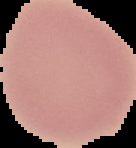

Summary:
  - Image size: 136×148 pixels
  - Malaria status: uninfected
  - Image type: cell region segmented out of the field of view; surrounding area masked to black
  - Preparation: thin blood smear